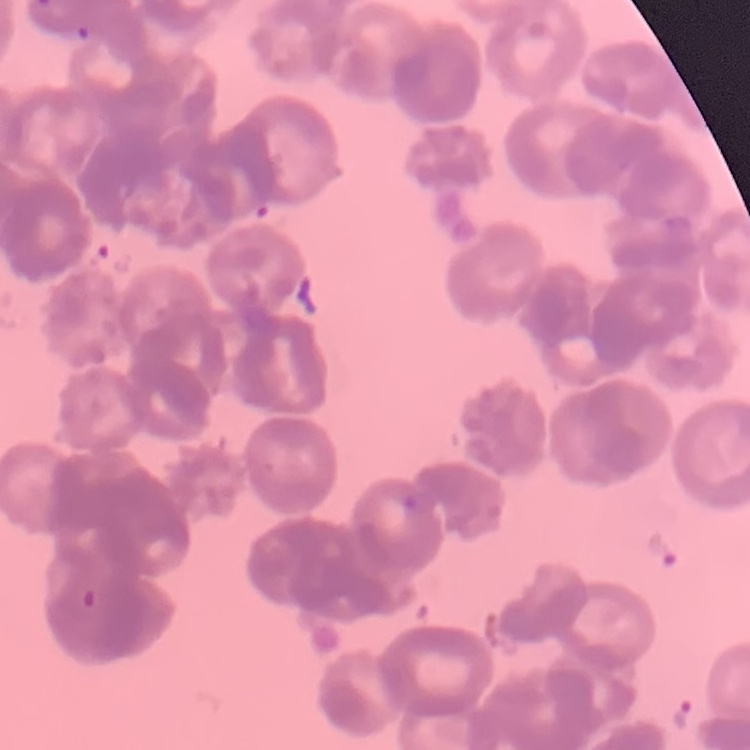
The erythrocytes exhibit rouleaux formation. One tile cut from a larger photomicrograph. Field's or Giemsa stain. Thin blood film.